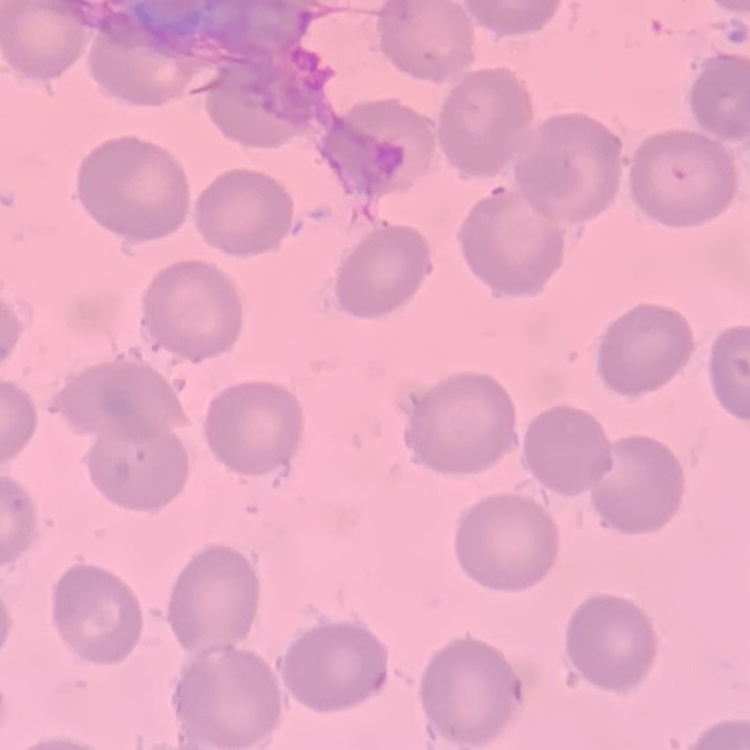

The red blood cells exhibit no rouleaux formation. Thin blood film. Square crop of a larger photomicrograph. Stained with either Field's or Giemsa.